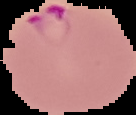

image size = 136×115 pixels
malaria status = parasitized
image type = segmented cell region with the area outside set to black
preparation = thin blood film